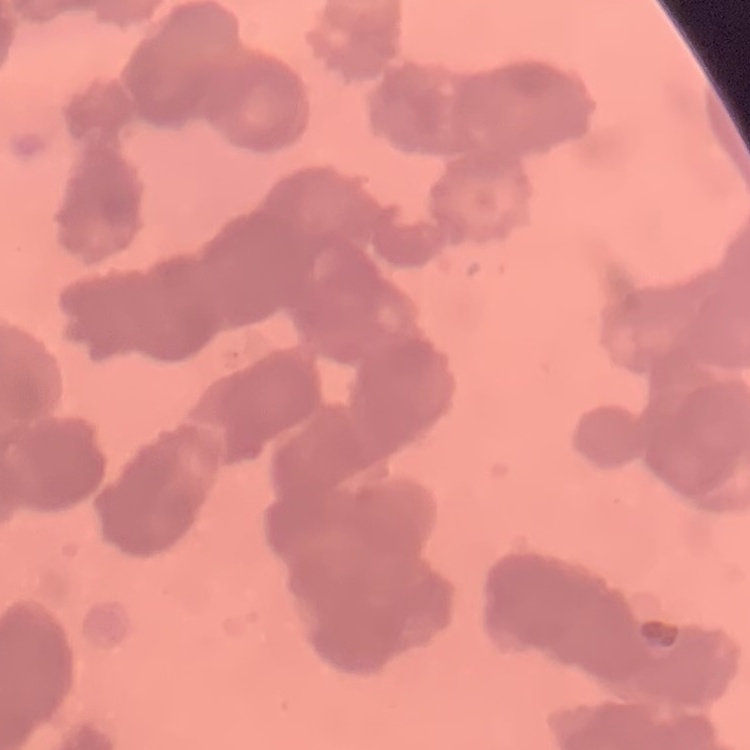
Summary:
  - Red blood cell morphology: rouleaux formation
  - Stain: Field's or Giemsa
  - Preparation: thin blood smear
  - Image type: square crop of a larger photomicrograph